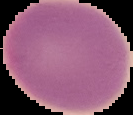
Image is 133×115 pixels. The area outside the segmented cell region is set to black. From a thin blood film. Malaria status: uninfected.